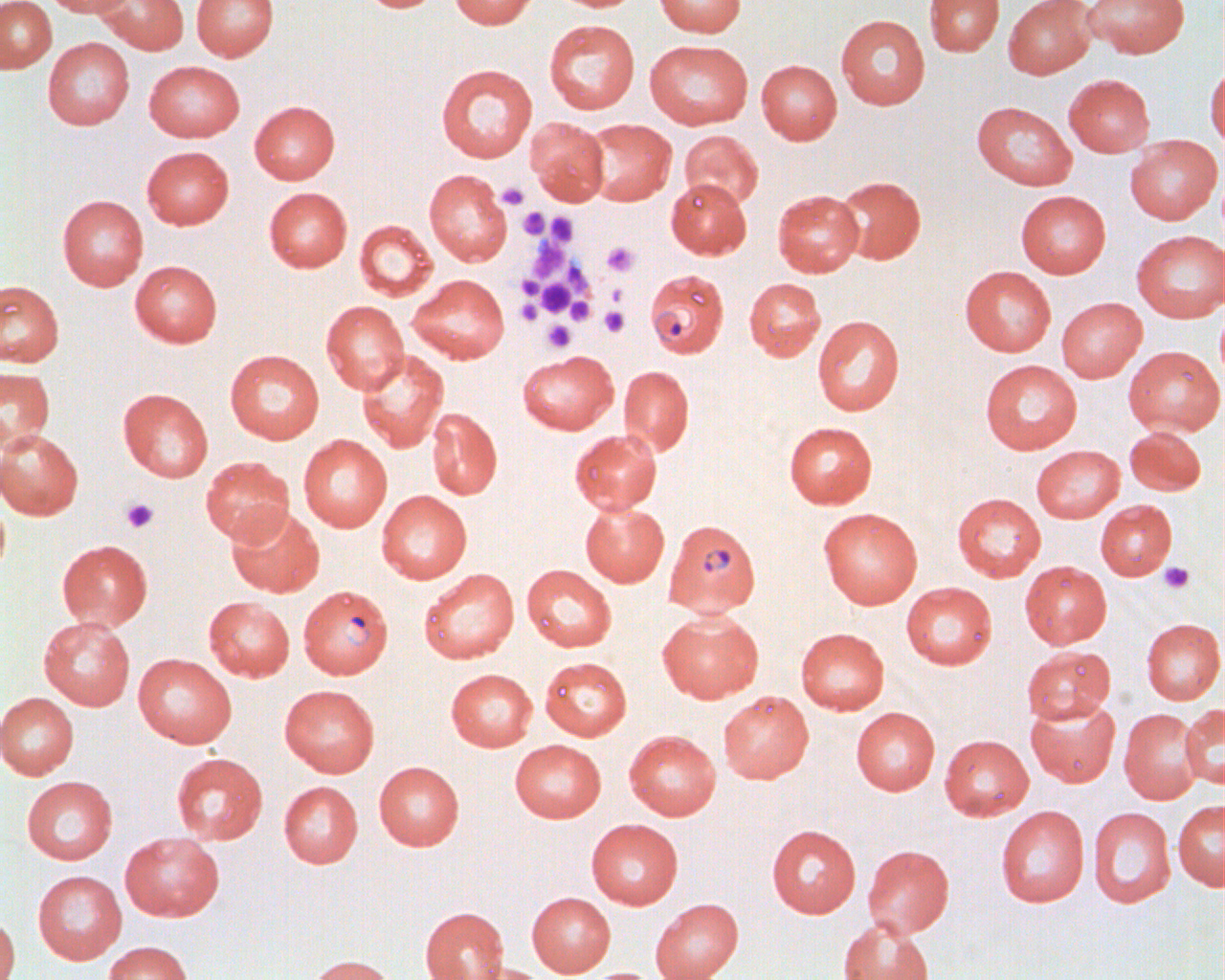
Summary:
  - Coordinate format: approximate bounding boxes as (x1, y1, x2, y2) in pixels
  - Uninfected red blood cell locations: (41, 0, 132, 17), (94, 0, 188, 54), (191, 0, 278, 61), (356, 0, 442, 12), (449, 0, 537, 29), (549, 0, 642, 12), (654, 0, 746, 37), (924, 0, 1004, 57), (1003, 0, 1096, 79), (1083, 0, 1189, 58), (0, 1, 56, 73), (835, 14, 930, 109), (544, 19, 640, 114), (43, 37, 134, 130), (644, 39, 753, 129), (756, 59, 842, 145), (144, 60, 244, 142), (436, 64, 537, 162), (1205, 65, 1225, 153), (1063, 74, 1155, 157), (249, 100, 340, 184), (971, 101, 1077, 190), (526, 117, 610, 206), (581, 118, 677, 206), (679, 130, 764, 210), (1124, 135, 1222, 225), (142, 146, 234, 230), (424, 169, 512, 266), (835, 176, 926, 264), (665, 178, 751, 259), (264, 187, 352, 272), (773, 189, 864, 277), (1016, 190, 1111, 278), (57, 194, 148, 290), (354, 219, 437, 301), (1131, 230, 1225, 322), (130, 260, 222, 347), (960, 265, 1057, 356), (408, 274, 509, 363), (744, 277, 826, 360), (0, 280, 63, 366), (1056, 297, 1147, 382), (1215, 299, 1225, 391), (321, 300, 408, 394), (812, 315, 904, 416), (1123, 345, 1224, 435), (224, 349, 324, 444), (356, 350, 449, 453), (517, 350, 618, 435), (980, 359, 1082, 454), (619, 365, 693, 455), (0, 366, 54, 453), (118, 388, 213, 481), (427, 408, 502, 500), (783, 421, 877, 509), (1124, 425, 1206, 496), (0, 428, 83, 520), (569, 429, 662, 514), (298, 435, 392, 532), (1031, 445, 1124, 523), (200, 456, 294, 545), (376, 490, 472, 584), (952, 493, 1046, 581), (0, 496, 10, 582), (1095, 500, 1177, 580), (580, 502, 669, 587), (225, 505, 324, 597), (817, 507, 922, 609), (57, 539, 153, 630), (1020, 561, 1111, 649), (522, 564, 616, 652), (419, 568, 519, 664), (901, 581, 997, 669), (203, 596, 295, 681), (657, 609, 764, 704), (38, 616, 135, 710), (1140, 618, 1225, 704), (795, 627, 889, 714), (1022, 646, 1115, 723), (133, 653, 236, 748), (540, 657, 632, 740), (446, 668, 537, 751), (279, 684, 379, 777), (718, 690, 813, 783), (0, 692, 79, 779), (1025, 696, 1120, 787), (1180, 703, 1225, 788), (851, 707, 939, 795), (1119, 708, 1204, 804), (624, 730, 721, 820), (940, 734, 1034, 820), (510, 739, 605, 822), (171, 752, 267, 844), (373, 761, 464, 850), (21, 776, 117, 865), (279, 781, 362, 867), (1173, 800, 1225, 890), (995, 805, 1089, 908), (1089, 807, 1175, 909), (586, 818, 683, 909), (766, 824, 861, 918), (119, 832, 224, 921), (863, 844, 954, 938), (32, 870, 127, 964), (527, 892, 615, 977), (650, 898, 743, 980), (420, 906, 509, 980), (0, 912, 20, 980), (837, 917, 934, 980), (102, 941, 193, 980), (303, 954, 397, 980), (461, 962, 552, 980), (581, 967, 661, 980)
  - Platelet locations: (497, 182, 529, 209), (518, 207, 549, 240), (546, 212, 578, 246), (527, 237, 570, 280), (601, 241, 639, 277), (568, 265, 593, 296), (517, 276, 543, 299), (538, 280, 573, 316), (604, 284, 624, 306), (566, 297, 593, 325), (516, 299, 543, 326), (599, 306, 629, 337), (543, 320, 575, 352), (121, 497, 159, 533), (1158, 563, 1194, 593)
  - Plasmodium falciparum-infected red blood cell locations: (645, 269, 729, 357), (663, 519, 761, 617), (298, 584, 393, 679)
  - Slide-level diagnosis: Plasmodium falciparum
  - Preparation: thin blood film
  - Modality: optical microscopy
  - Magnification: 1000x
  - Image size: 1225×980 pixels
  - Field of view: one of a larger specimen